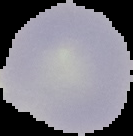

Segmented cell region on a black background. Malaria status: uninfected. From a thin blood film. Image is 133×136 pixels.